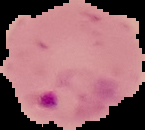
Summary:
  - Image type: segmented cell region with the area outside set to black
  - Preparation: thin blood film
  - Result: Plasmodium parasites identified
  - Image size: 145×130 pixels